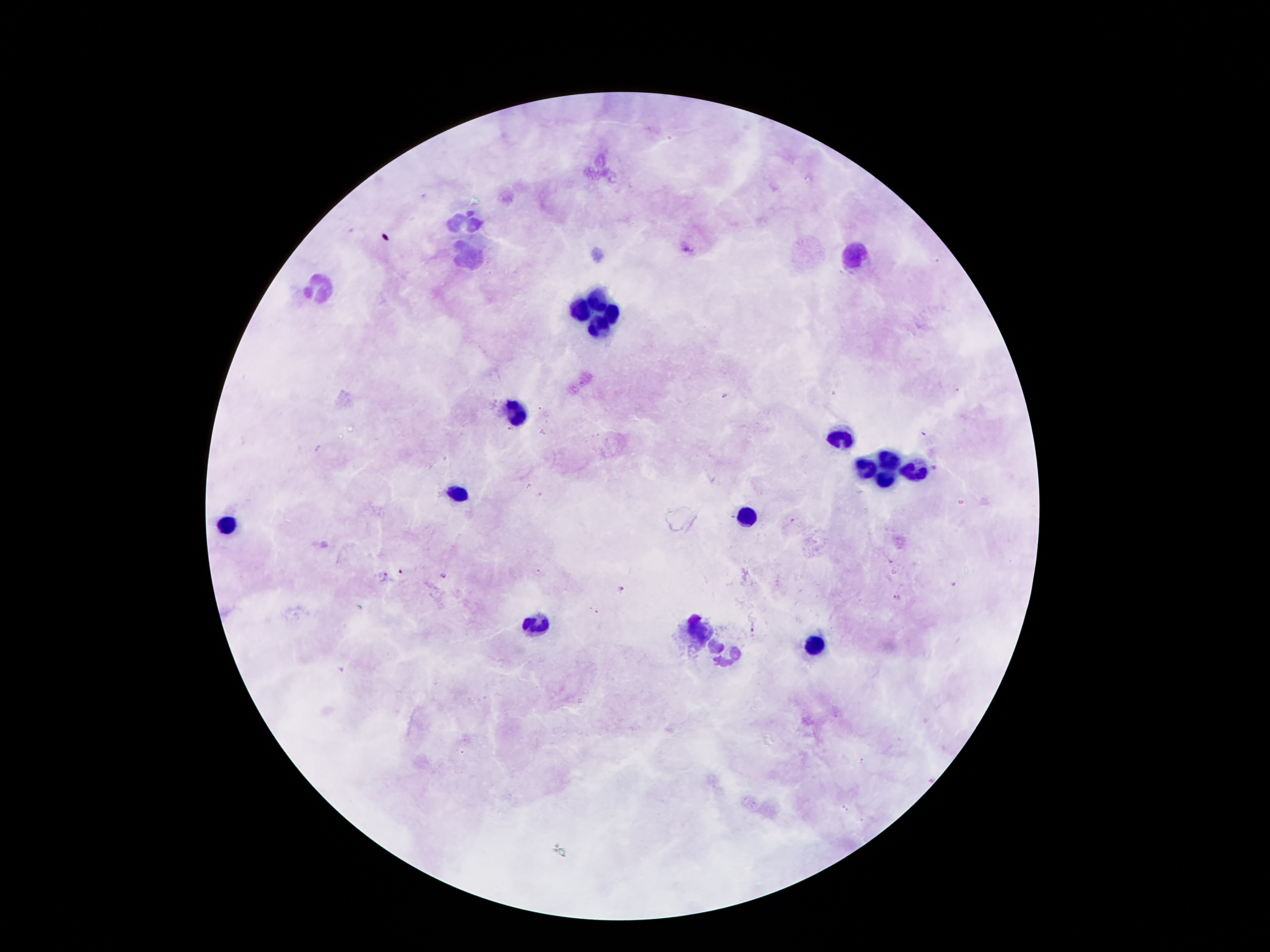

Giemsa-stained preparation. Patient malaria status: positive for Plasmodium falciparum. One field from this slide. Smartphone photograph taken through the microscope eyepiece. Image is 1270×952 pixels. 100x magnification. Thick peripheral-blood smear.